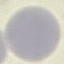

Malaria status: uninfected. Giemsa stain. Automatically extracted cell patch, resized to 64 × 64 pixels. Acquired by smartphone through the microscope eyepiece. Thin smear of blood.